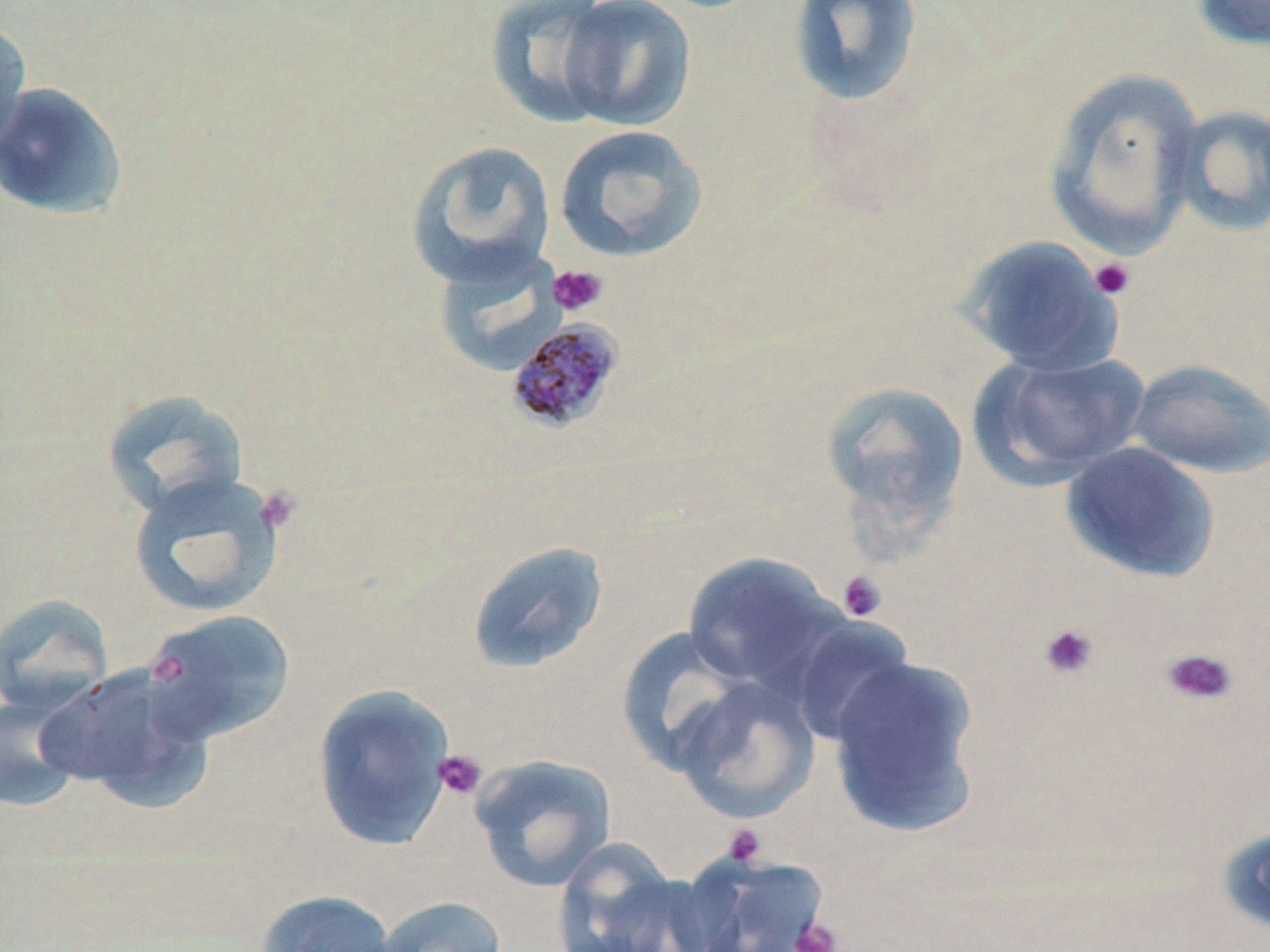

Plasmodium malariae-infected red blood cell locations = approximate bounding boxes as (x1,y1)-(x2,y2) corner pairs in pixels: (504,318)-(626,434)
slide-level diagnosis = Plasmodium malariae
preparation = thin blood film
stain = May-Grünwald-Giemsa
platelet locations = approximate bounding boxes as (x1,y1)-(x2,y2) corner pairs in pixels: (1088,257)-(1136,301), (548,264)-(608,316), (253,485)-(302,536), (836,570)-(887,622), (1038,623)-(1099,679), (1162,647)-(1239,706), (149,652)-(186,686), (433,749)-(487,801), (722,824)-(767,866), (789,918)-(843,952)
magnification = 1000x
image size = 1270×952 pixels
field of view = one of a larger specimen
uninfected red blood cell locations = approximate bounding boxes as (x1,y1)-(x2,y2) corner pairs in pixels: (484,0)-(622,128), (555,0)-(698,131), (787,0)-(924,109), (1190,0)-(1270,52), (0,16)-(33,157), (1043,69)-(1203,257), (0,82)-(129,219), (1172,104)-(1269,237), (554,124)-(708,263), (405,140)-(556,287), (957,234)-(1125,376), (431,245)-(567,378), (970,351)-(1149,487), (1127,358)-(1270,479), (821,381)-(970,534), (101,388)-(250,519), (1060,441)-(1220,584), (127,471)-(287,618), (466,540)-(609,675), (683,553)-(847,699), (0,593)-(114,715), (139,609)-(297,747), (786,618)-(913,747), (616,627)-(751,774), (826,655)-(982,837), (37,664)-(210,807), (669,675)-(821,824), (311,684)-(458,852), (0,690)-(86,813), (469,754)-(618,892), (552,837)-(697,952), (679,851)-(831,951), (256,889)-(399,952), (373,895)-(508,952)
modality = optical microscopy